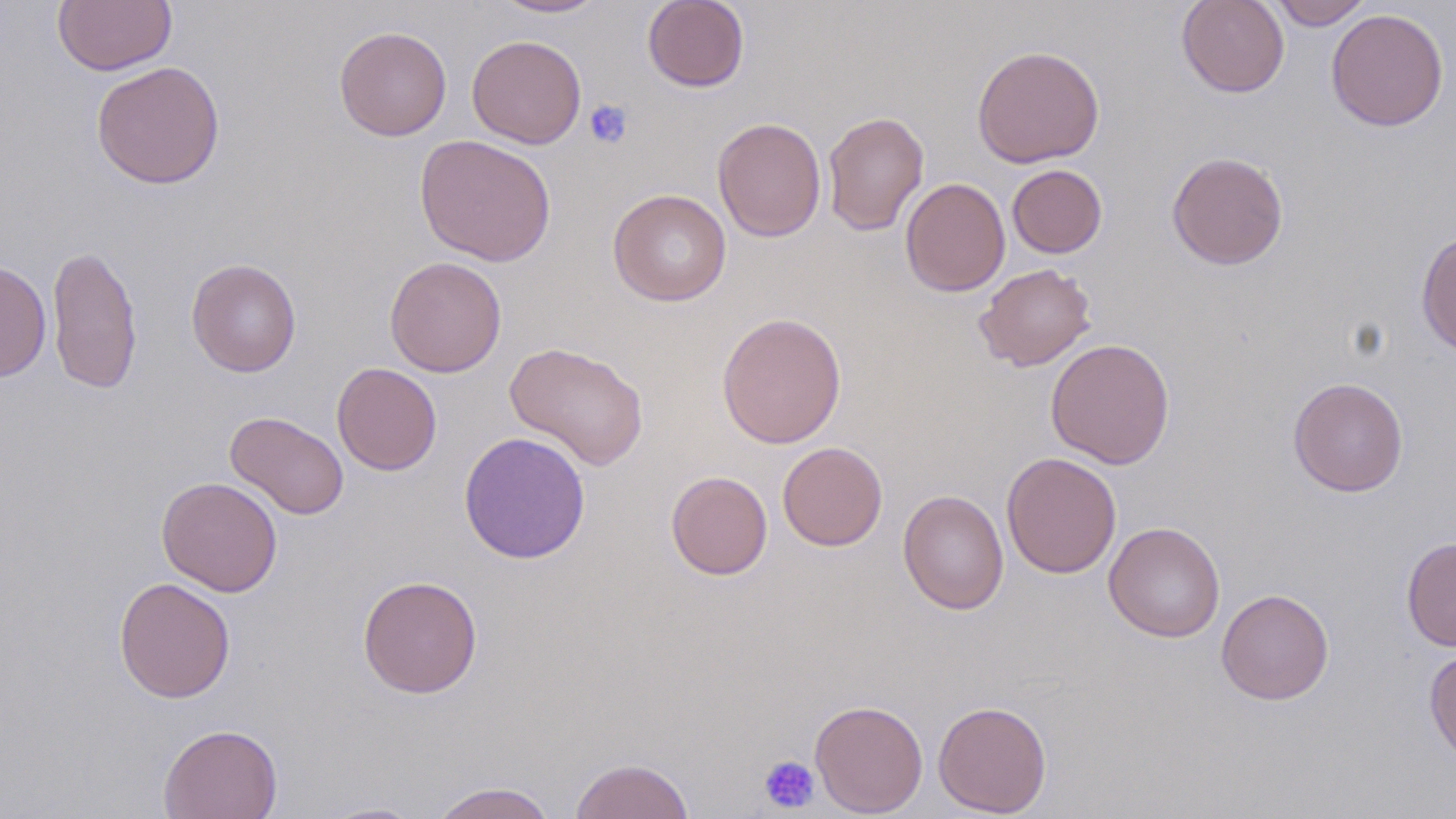
Summary:
  - Coordinate format: approximate bounding boxes as (x1, y1, x2, y2) in pixels
  - Platelet locations: (584, 99, 633, 149), (758, 755, 820, 813)
  - Uninfected red blood cell locations: (52, 0, 176, 76), (492, 0, 608, 18), (642, 0, 750, 92), (1177, 0, 1290, 98), (1266, 0, 1374, 29), (1326, 8, 1449, 131), (334, 25, 452, 141), (466, 34, 587, 149), (971, 45, 1105, 168), (91, 60, 225, 189), (822, 110, 929, 236), (712, 117, 826, 242), (414, 134, 557, 266), (1166, 151, 1289, 270), (1007, 164, 1108, 258), (900, 177, 1010, 297), (607, 189, 732, 306), (1416, 229, 1455, 357), (47, 243, 143, 395), (384, 256, 507, 378), (186, 258, 302, 377), (0, 260, 51, 382), (974, 263, 1096, 371), (716, 311, 847, 449), (1045, 338, 1175, 469), (504, 340, 650, 472), (332, 362, 442, 475), (1288, 376, 1409, 497), (225, 410, 349, 521), (458, 432, 591, 564), (777, 442, 888, 551), (1002, 452, 1121, 578), (666, 471, 773, 580), (156, 477, 283, 597), (897, 489, 1009, 615), (1103, 521, 1226, 642), (1401, 536, 1456, 651), (357, 574, 483, 698), (114, 576, 236, 703), (1216, 588, 1334, 705), (1424, 647, 1456, 763), (809, 699, 928, 817), (933, 700, 1052, 816), (158, 723, 283, 819), (569, 757, 696, 819), (429, 781, 558, 819), (315, 801, 430, 818)
  - Slide-level diagnosis: negative for blood parasites
  - Image size: 1456×819 pixels
  - Modality: light microscopy
  - Magnification: 1000x
  - Preparation: thin blood smear
  - Field of view: single
  - Stain: May-Grünwald-Giemsa